Comment on the morphology of the red blood cells.
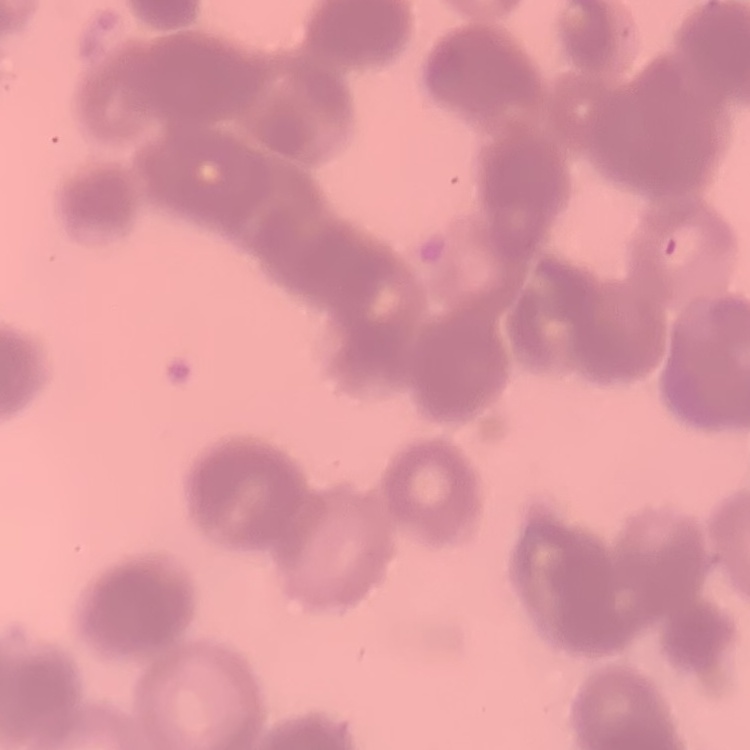
They show rouleaux formation.

One tile cut from a larger photomicrograph. Stained with either Field's or Giemsa. Thin blood film.